Outline each blood parasite and name the species.
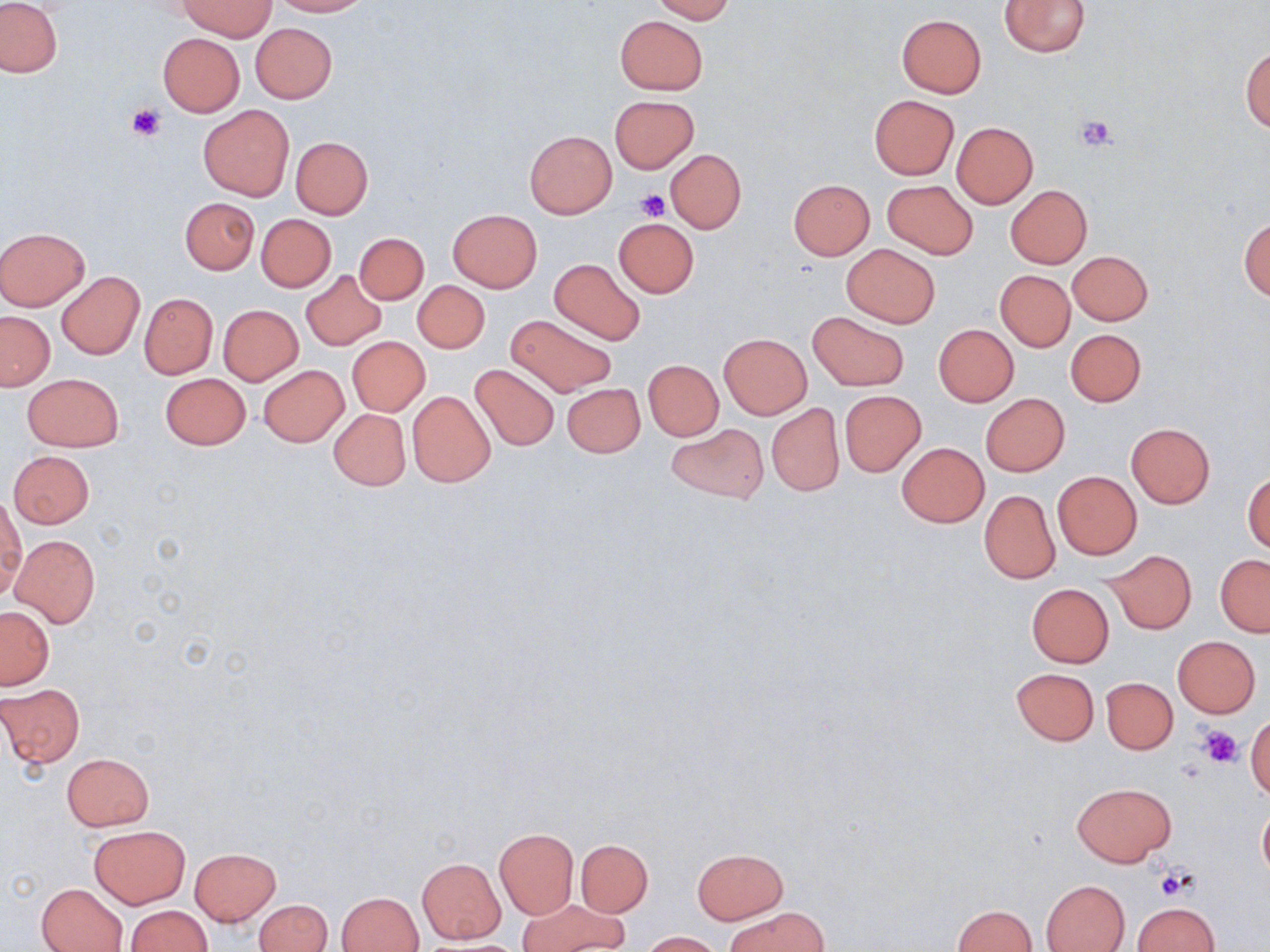
No blood parasites observed.

{
  "slide_level_diagnosis": "negative for blood parasites",
  "modality": "light microscopy",
  "magnification": "1000x",
  "uninfected_red_blood_cell_locations": "approximate bounding boxes as [x1, y1, x2, y2] in pixels: [272, 0, 370, 16], [650, 0, 734, 22], [999, 0, 1091, 57], [0, 1, 63, 78], [180, 1, 274, 40], [614, 14, 710, 94], [895, 14, 986, 98], [250, 23, 336, 103], [157, 33, 245, 116], [1241, 46, 1270, 132], [609, 95, 699, 173], [869, 95, 959, 179], [198, 105, 295, 201], [951, 121, 1039, 208], [526, 131, 616, 217], [291, 136, 373, 218], [666, 149, 746, 234], [789, 180, 874, 259], [881, 180, 977, 258], [1005, 184, 1092, 269], [180, 197, 259, 274], [449, 210, 542, 292], [257, 215, 336, 291], [613, 218, 699, 297], [1239, 218, 1269, 300], [0, 227, 90, 310], [354, 232, 429, 306], [842, 243, 940, 327], [1067, 250, 1153, 326], [549, 258, 646, 345], [299, 269, 388, 350], [996, 270, 1075, 351], [57, 272, 144, 359], [412, 281, 489, 353], [139, 293, 217, 379], [218, 305, 302, 385], [808, 311, 908, 390], [0, 312, 54, 389], [507, 314, 618, 397], [933, 324, 1018, 406], [1066, 329, 1145, 406], [720, 334, 811, 418], [347, 337, 429, 416], [643, 360, 723, 440], [258, 364, 349, 448], [469, 364, 560, 450], [23, 373, 123, 451], [160, 373, 251, 450], [561, 383, 646, 457], [407, 390, 496, 487], [839, 390, 926, 475], [981, 393, 1070, 476], [766, 402, 844, 495], [328, 408, 410, 490], [1125, 422, 1215, 508], [667, 423, 767, 504], [896, 442, 990, 527], [9, 451, 94, 528], [1052, 470, 1142, 559], [1243, 471, 1270, 554], [980, 490, 1059, 584], [0, 494, 24, 598], [10, 534, 100, 627], [1103, 550, 1197, 634], [1216, 554, 1270, 636], [1026, 583, 1114, 667], [0, 607, 53, 688], [1173, 636, 1261, 717], [1011, 667, 1099, 746], [1101, 677, 1177, 754], [0, 684, 85, 768], [1247, 712, 1270, 801], [62, 754, 153, 831], [1073, 783, 1174, 865], [1258, 800, 1270, 884], [89, 824, 189, 908], [494, 828, 578, 919], [576, 839, 652, 916], [190, 848, 280, 925], [692, 848, 787, 924], [418, 859, 505, 942], [1042, 880, 1128, 952], [37, 882, 128, 951], [338, 892, 424, 952], [254, 899, 331, 952], [519, 899, 626, 951], [1133, 901, 1221, 952], [124, 905, 212, 951], [952, 905, 1036, 952], [729, 906, 827, 951], [640, 931, 722, 951]",
  "stain": "May-Grünwald-Giemsa",
  "field_of_view": "single",
  "preparation": "thin blood film",
  "image_size": "1270×952 pixels",
  "platelet_locations": "approximate bounding boxes as [x1, y1, x2, y2] in pixels: [127, 102, 167, 141], [1073, 113, 1118, 152], [636, 190, 669, 222], [1197, 724, 1243, 766], [1154, 865, 1194, 898]"
}